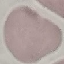

Summary:
  - Result: negative for malaria parasites
  - Preparation: thin smear
  - Image type: cell patch, automatically extracted from a larger field of view and resized to 64 × 64 pixels
  - Capture: smartphone through the microscope eyepiece
  - Stain: Giemsa